Give the position of every malaria parasite.
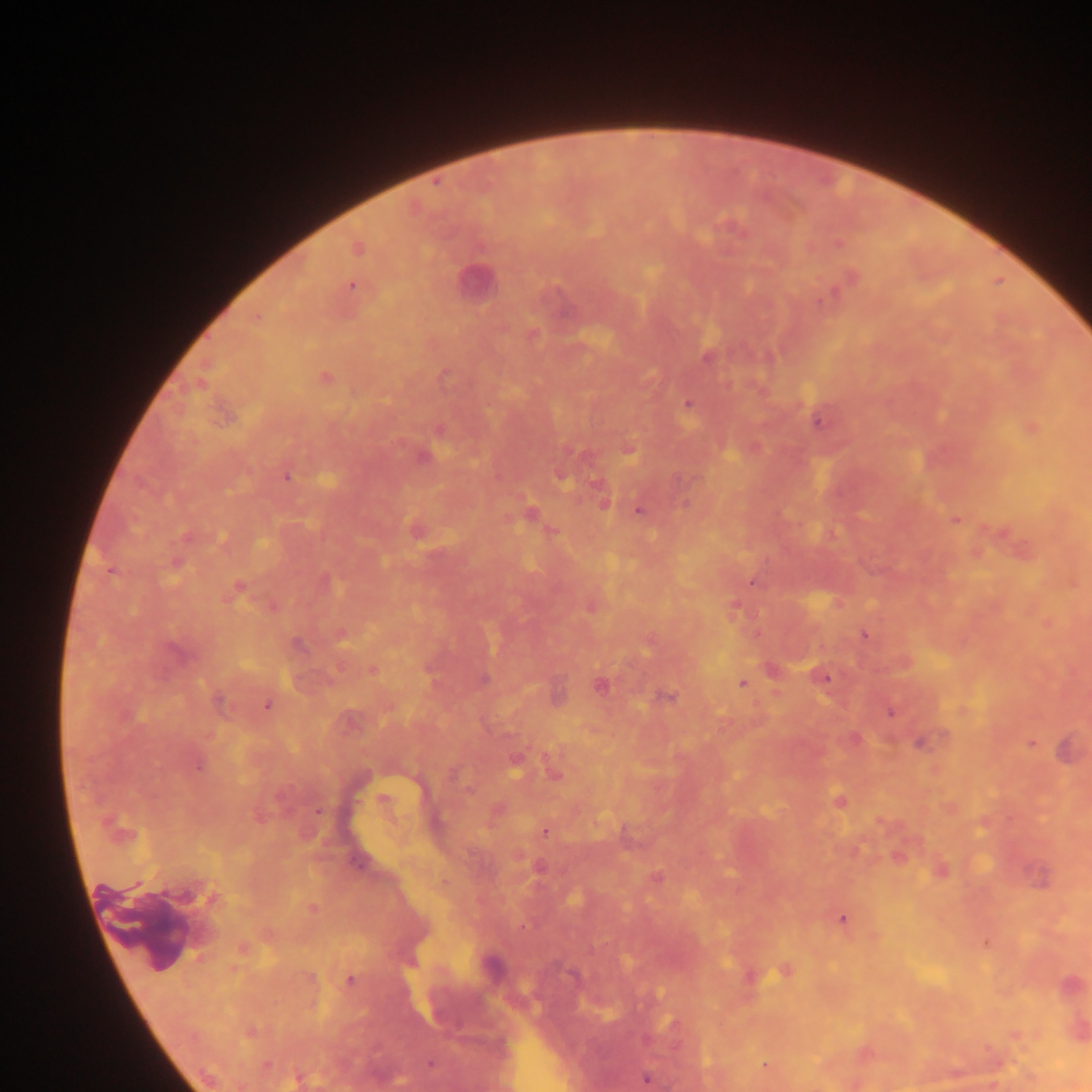

Approximate centers as [x, y] in pixels.
Malaria parasites: [729, 227], [838, 242], [357, 247], [850, 278], [350, 285], [255, 318], [531, 335], [708, 356], [444, 375], [323, 377], [688, 404], [818, 418], [1031, 427], [439, 430], [627, 448], [422, 456], [286, 476], [603, 501], [639, 509], [530, 514], [955, 519], [415, 529], [552, 530], [1000, 533], [176, 563], [753, 580], [238, 586], [272, 605], [591, 605], [734, 608], [1047, 623], [340, 633], [864, 634], [372, 669], [820, 676], [482, 679], [742, 684], [599, 685], [556, 697], [665, 697], [219, 703], [267, 704], [890, 711], [921, 741], [1031, 742], [1067, 749], [515, 762], [197, 764], [553, 772], [382, 800], [839, 801], [319, 811], [495, 811], [546, 831], [897, 855], [539, 868], [939, 870], [1038, 877], [655, 878], [312, 908], [843, 918], [985, 942], [242, 948], [490, 965], [786, 971], [749, 976], [350, 980], [1070, 986], [1077, 1029], [249, 1032], [1015, 1035], [864, 1053], [431, 1065], [765, 1066], [646, 1078], [298, 1079].

image size = 1092×1092 pixels
field of view = single
capture = mobile-phone photograph through a microscope
preparation = thick blood film
leukocyte locations = approximate centers as [x, y] in pixels: [474, 280]
country = Ghana